Assess this cell for malaria.
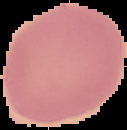
It is uninfected.

Summary:
  - Image type: cell region segmented out of the field of view; surrounding area masked to black
  - Preparation: thin blood smear
  - Image size: 127×130 pixels